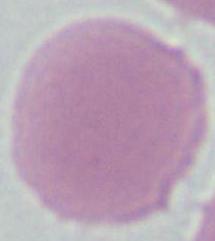

1000x magnification. Photomicrograph. An erythrocyte is shown.